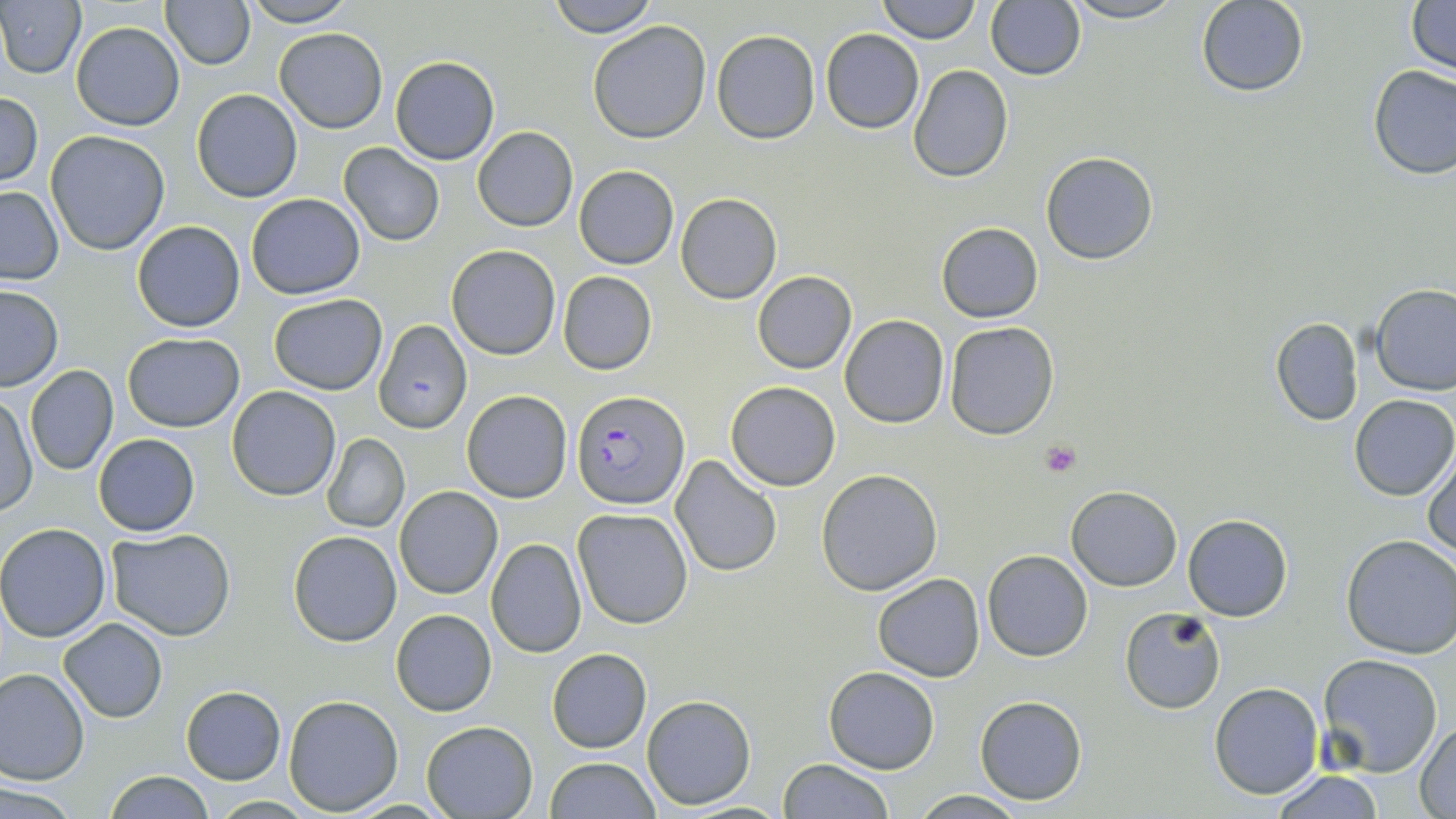
slide-level diagnosis = Plasmodium falciparum
preparation = thin blood film
Plasmodium falciparum-infected red blood cell locations = approximate bounding boxes as (x1,y1)-(x2,y2) corner pairs in pixels: (374,322)-(473,438), (573,391)-(687,510)
modality = light microscopy
magnification = 1000x
platelet locations = approximate bounding boxes as (x1,y1)-(x2,y2) corner pairs in pixels: (1039,439)-(1081,478)
stain = May-Grünwald-Giemsa
image size = 1456×819 pixels
field of view = one of a larger specimen
uninfected red blood cell locations = approximate bounding boxes as (x1,y1)-(x2,y2) corner pairs in pixels: (241,0)-(356,27), (548,0)-(658,37), (877,0)-(979,43), (1060,0)-(1187,24), (1196,0)-(1309,96), (1406,0)-(1455,75), (161,1)-(255,70), (985,1)-(1085,81), (1,3)-(84,78), (71,21)-(185,131), (587,21)-(711,143), (275,28)-(388,132), (821,28)-(924,132), (712,29)-(821,145), (391,56)-(499,165), (908,65)-(1013,181), (1367,65)-(1455,179), (192,89)-(302,202), (0,92)-(42,187), (473,127)-(578,230), (46,130)-(171,256), (338,143)-(444,247), (1041,152)-(1159,264), (574,166)-(679,269), (0,186)-(64,285), (675,193)-(782,303), (245,194)-(365,299), (131,220)-(246,333), (936,222)-(1043,321), (446,245)-(562,360), (753,271)-(856,373), (557,272)-(657,375), (0,286)-(63,391), (1372,286)-(1456,396), (269,293)-(387,395), (840,315)-(949,428), (1271,317)-(1364,426), (944,321)-(1061,440), (122,333)-(246,432), (24,365)-(118,477), (725,382)-(841,491), (227,386)-(341,500), (461,390)-(573,503), (1350,393)-(1456,500), (1,397)-(37,514), (93,433)-(200,537), (322,434)-(408,533), (1424,453)-(1456,557), (670,454)-(783,576), (816,469)-(943,594), (394,486)-(502,598), (1065,486)-(1182,590), (571,507)-(694,630), (1183,515)-(1292,621), (0,523)-(113,642), (108,528)-(236,640), (288,531)-(402,646), (1339,534)-(1456,660), (486,538)-(586,657), (982,549)-(1094,661), (873,573)-(985,682), (390,609)-(497,715), (1121,610)-(1227,712), (59,618)-(168,723), (547,649)-(652,752), (1317,653)-(1444,777), (825,666)-(939,773), (0,667)-(90,784), (1210,683)-(1324,800), (181,687)-(286,784), (975,694)-(1087,804), (284,695)-(403,815), (641,695)-(757,808), (1415,718)-(1455,817), (421,720)-(540,818), (545,756)-(660,819), (779,759)-(893,818), (1266,769)-(1387,818), (104,770)-(215,819), (2,781)-(82,816), (911,790)-(1027,818), (207,795)-(319,817)